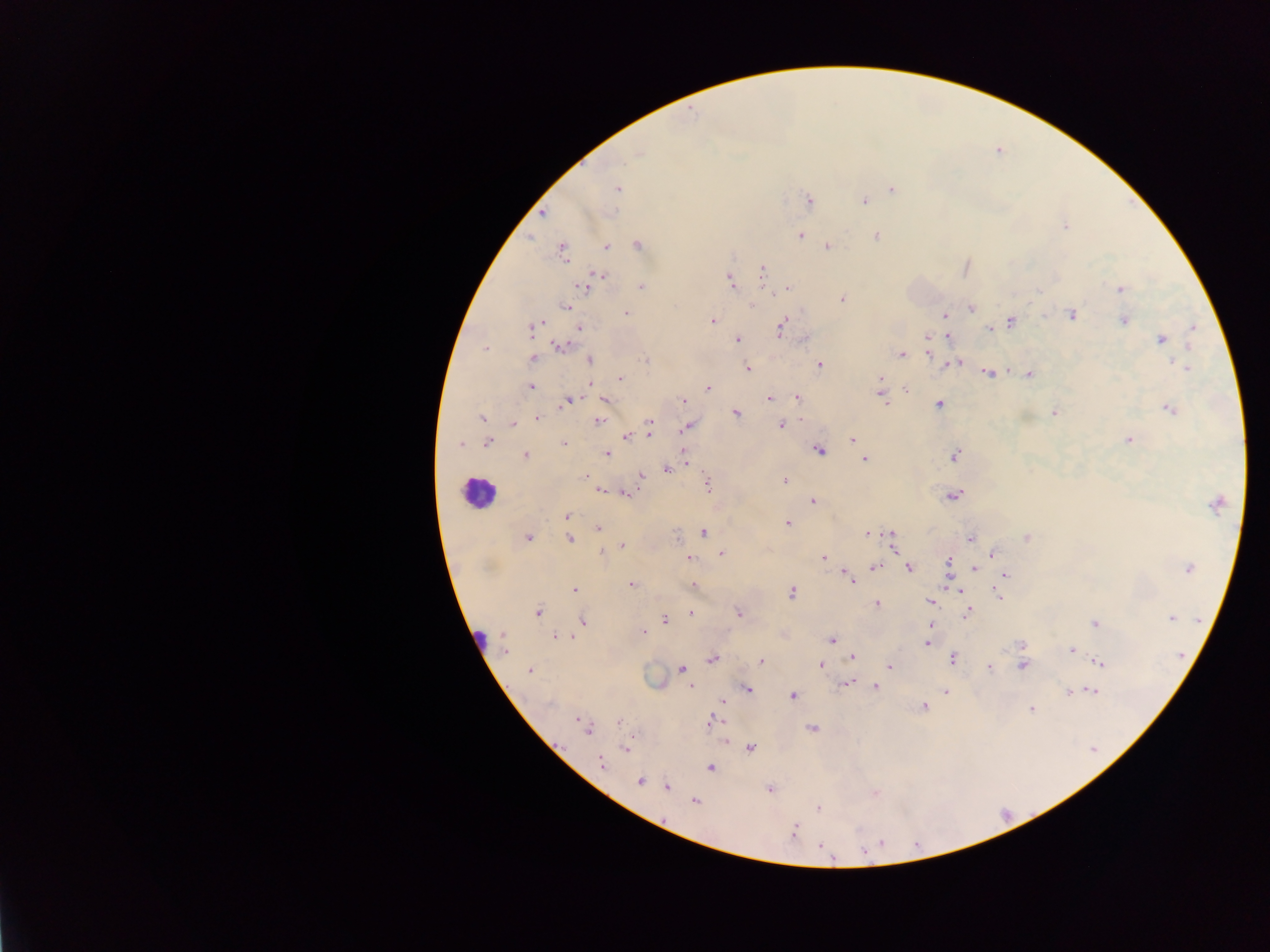

Approximate centers as (x, y) in pixels. Malaria parasite locations: (637, 153), (617, 188), (892, 189), (808, 200), (864, 200), (542, 213), (1064, 226), (799, 235), (876, 236), (638, 244), (605, 246), (827, 246), (562, 251), (762, 269), (600, 275), (595, 278), (730, 280), (584, 285), (641, 286), (788, 288), (1121, 289), (842, 298), (567, 306), (752, 306), (970, 307), (625, 313), (944, 315), (1072, 315), (712, 320), (1123, 320), (1011, 321), (532, 327), (579, 327), (783, 327), (1193, 328), (989, 330), (927, 336), (949, 337), (1162, 338), (736, 339), (560, 346), (1189, 346), (486, 348), (930, 352), (901, 354), (533, 359), (589, 360), (956, 362), (818, 364), (949, 365), (747, 368), (1187, 368), (988, 372), (1029, 374), (619, 378), (880, 380), (589, 384), (530, 387), (708, 388), (880, 389), (906, 389), (882, 396), (798, 397), (605, 398), (769, 398), (567, 400), (683, 400), (884, 403), (938, 403), (1169, 408), (735, 412), (1054, 412), (481, 417), (538, 418), (598, 421), (512, 424), (780, 424), (686, 426), (648, 428), (626, 436), (852, 439), (1129, 439), (487, 442), (564, 443), (460, 444), (819, 449), (524, 454), (606, 454), (955, 455), (864, 459), (685, 460), (666, 469), (640, 474), (784, 481), (707, 484), (599, 489), (624, 492), (953, 495), (812, 502), (1217, 502), (567, 516), (788, 522), (598, 527), (703, 533), (866, 533), (527, 537), (1026, 537), (569, 538), (971, 538), (892, 541), (621, 546), (600, 552), (721, 553), (992, 554), (688, 558), (824, 558), (948, 561), (874, 567), (909, 568), (973, 568), (1187, 568), (846, 572), (948, 573), (1004, 573), (850, 581), (631, 584), (692, 586), (954, 587), (574, 589), (961, 591), (791, 593), (999, 595), (930, 601), (877, 604), (968, 611), (537, 612), (690, 613), (739, 613), (1171, 617), (664, 619), (583, 620), (1095, 623), (930, 624), (644, 631), (555, 636), (571, 636), (832, 639), (926, 643), (504, 644), (1021, 644), (1073, 649), (853, 656), (952, 658), (712, 659), (761, 661), (1099, 663), (820, 665), (1022, 665), (889, 666), (989, 667), (529, 669), (681, 669), (847, 682), (691, 686), (876, 687), (746, 688), (1090, 689), (946, 691), (1068, 692), (792, 695), (723, 701), (923, 706), (1032, 710), (619, 722), (711, 722), (586, 726), (812, 727), (725, 741), (750, 747), (627, 748), (601, 763), (709, 767), (639, 781), (667, 786), (769, 789), (695, 801), (818, 808), (793, 832). Leukocyte locations: (479, 495). Object labeled both malaria parasite and leukocyte by the source: (479, 639). Image is 1270×952 pixels. One field of view. Photographed through a microscope with a mobile-phone camera. Thick blood film. Collected in Ghana.